Give the extent of all uninfected red blood cells.
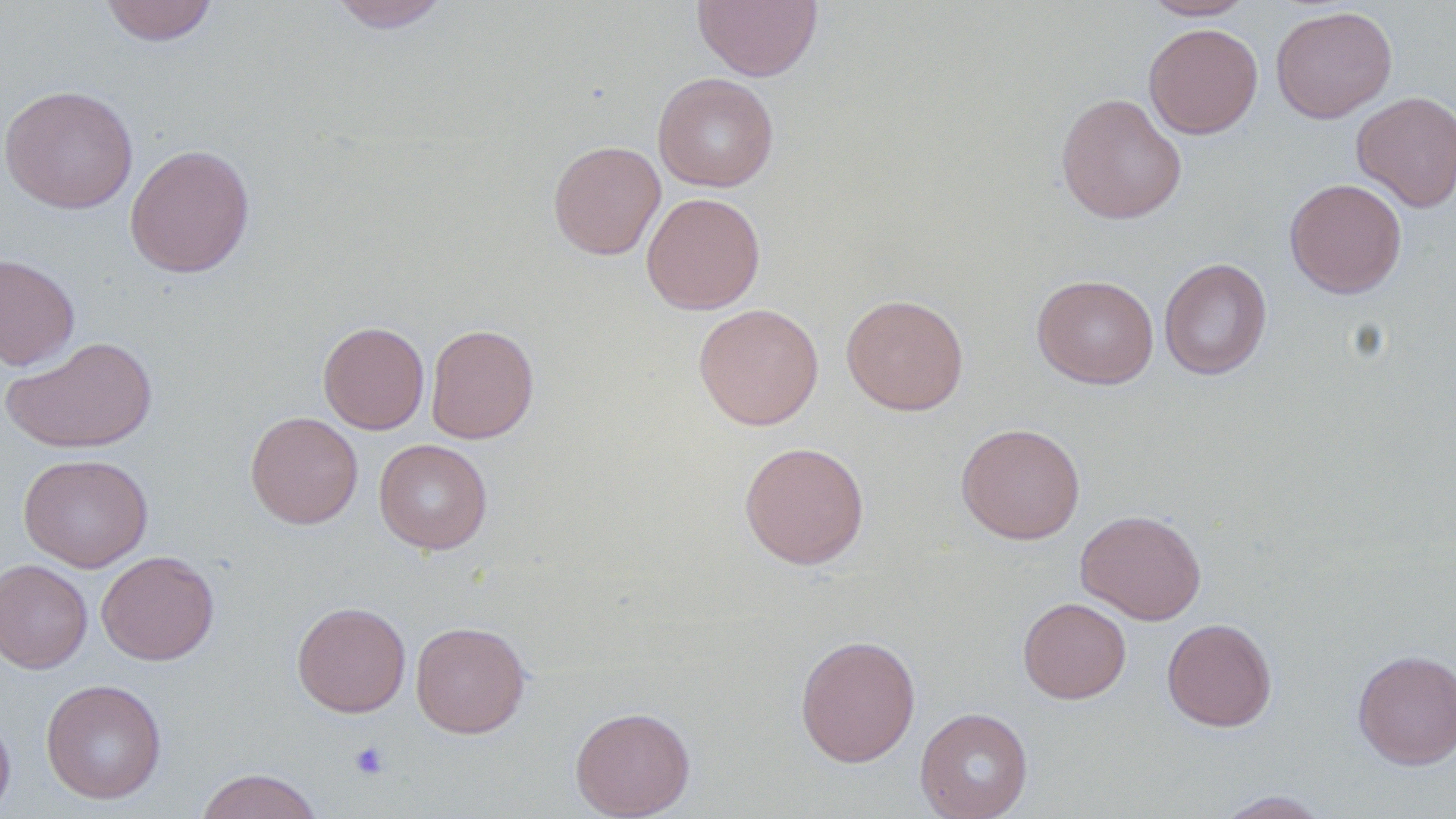
Approximate bounding boxes as (x1, y1, x2, y2) in pixels.
Uninfected red blood cells: (100, 0, 219, 45), (327, 0, 453, 32), (692, 0, 823, 82), (1141, 0, 1255, 20), (1270, 5, 1397, 124), (1144, 23, 1263, 139), (653, 72, 779, 192), (0, 84, 139, 214), (1351, 91, 1456, 212), (1055, 92, 1187, 224), (548, 140, 666, 260), (125, 143, 255, 278), (1284, 178, 1407, 298), (641, 192, 766, 314), (0, 251, 80, 371), (1159, 257, 1273, 381), (1032, 273, 1159, 389), (841, 293, 969, 416), (693, 303, 824, 430), (318, 320, 430, 434), (425, 323, 539, 444), (2, 335, 158, 454), (245, 411, 362, 529), (956, 422, 1085, 544), (374, 438, 492, 554), (739, 441, 870, 569), (18, 453, 153, 572), (1075, 508, 1207, 625), (97, 551, 220, 665), (0, 558, 92, 673), (1018, 597, 1131, 704), (292, 600, 411, 718), (1161, 617, 1277, 732), (410, 621, 530, 738), (794, 634, 921, 767), (1353, 648, 1456, 769), (40, 678, 167, 804), (570, 705, 695, 819), (915, 707, 1033, 819), (0, 709, 16, 819), (195, 767, 324, 819), (1214, 790, 1333, 818).

slide-level diagnosis = no evidence of blood parasites
preparation = thin blood smear
field of view = one of a larger specimen
platelet locations = approximate bounding boxes as (x1, y1, x2, y2) in pixels: (350, 741, 389, 779)
modality = light microscopy
image size = 1456×819 pixels
stain = May-Grünwald-Giemsa
magnification = 1000x